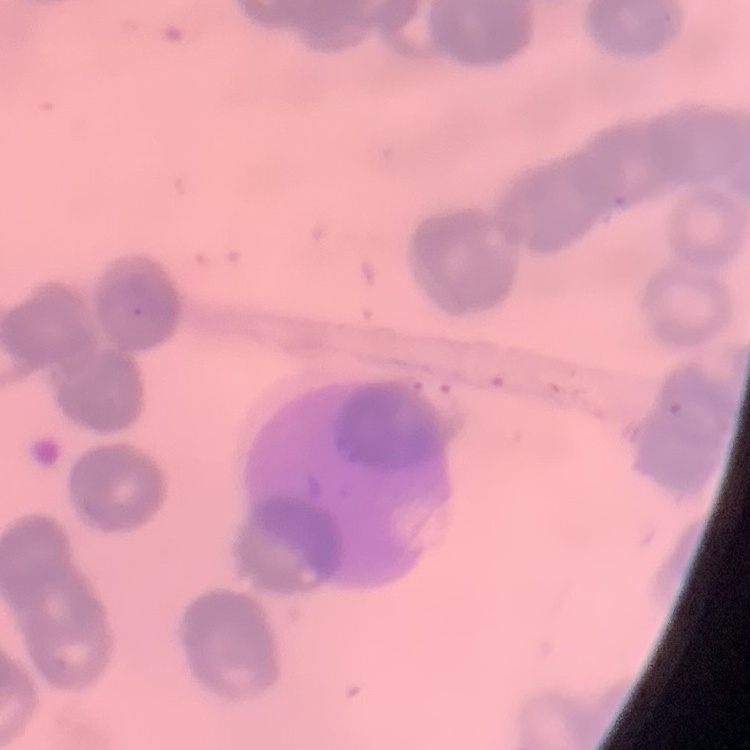

Summary:
  - Red blood cell morphology: rouleaux formation
  - Image type: one tile cut from a larger photomicrograph
  - Stain: Field's or Giemsa
  - Preparation: thin blood film